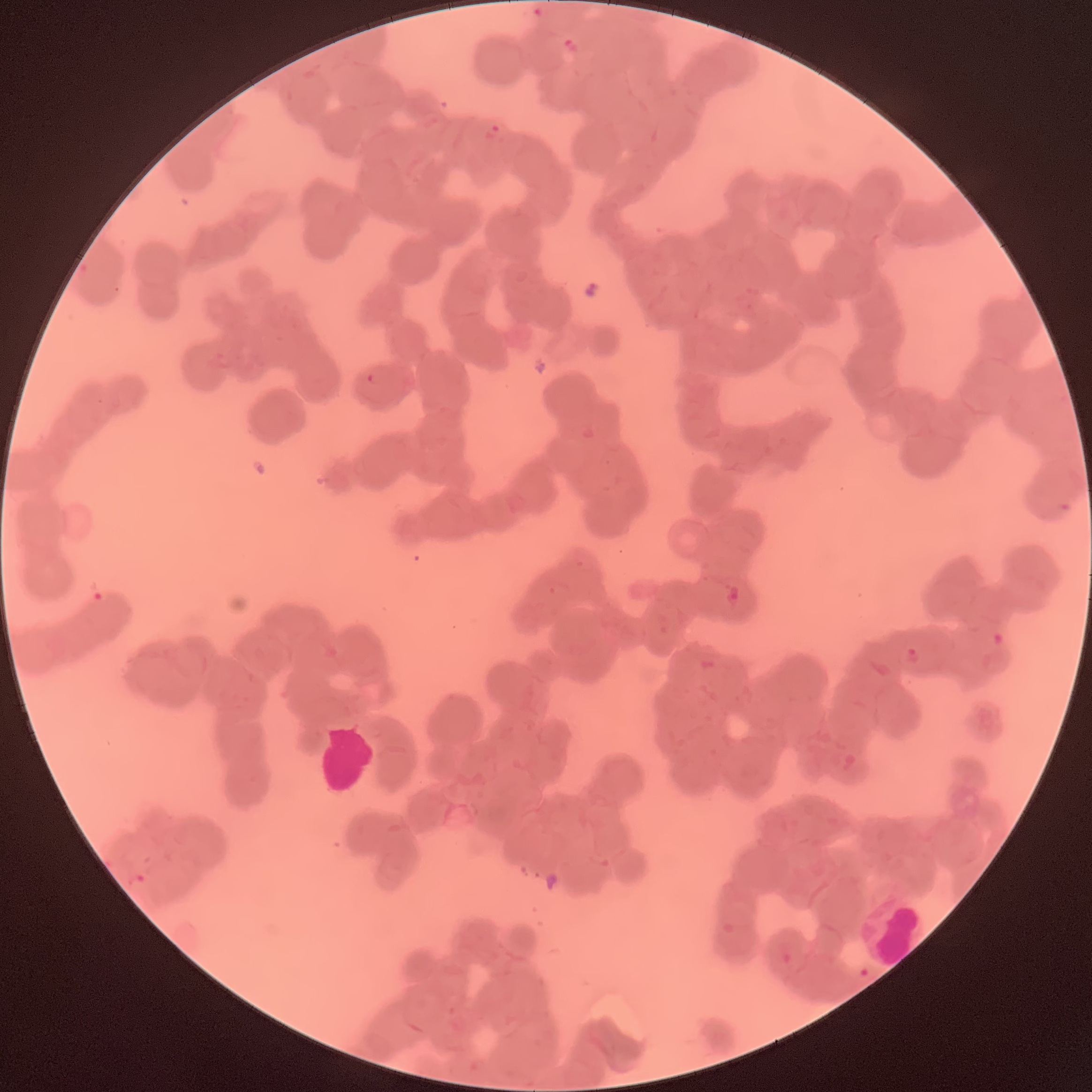

coordinate format = approximate bounding boxes as named x1/y1/x2/y2 corners in pixels
Plasmodium parasite locations = (x1=530, y1=6, x2=552, y2=23), (x1=563, y1=35, x2=581, y2=54), (x1=483, y1=123, x2=510, y2=146), (x1=366, y1=372, x2=382, y2=387), (x1=724, y1=584, x2=742, y2=607), (x1=991, y1=631, x2=1006, y2=648), (x1=902, y1=646, x2=921, y2=664)
image size = 1092×1092 pixels
preparation = thin blood film
modality = optical microscopy
red blood cell morphology = rouleaux formation